State which cell type is depicted.
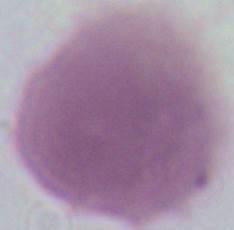
An erythrocyte.

1000x magnification. Micrograph.